Comment on the morphology of the erythrocytes.
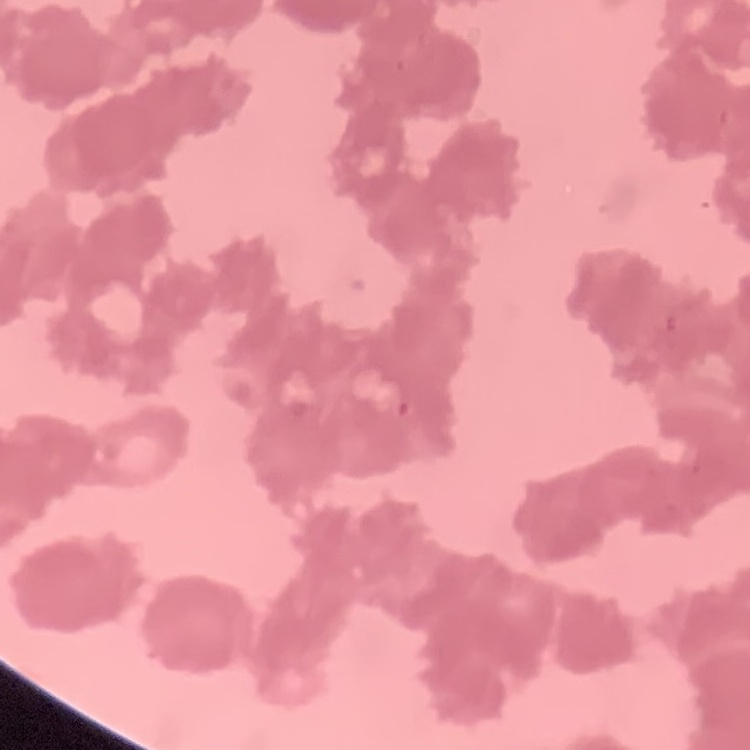

Rouleaux formation.

{
  "image_type": "square crop of a larger photomicrograph",
  "preparation": "thin blood smear",
  "stain": "Field's or Giemsa"
}